State the preparation type.
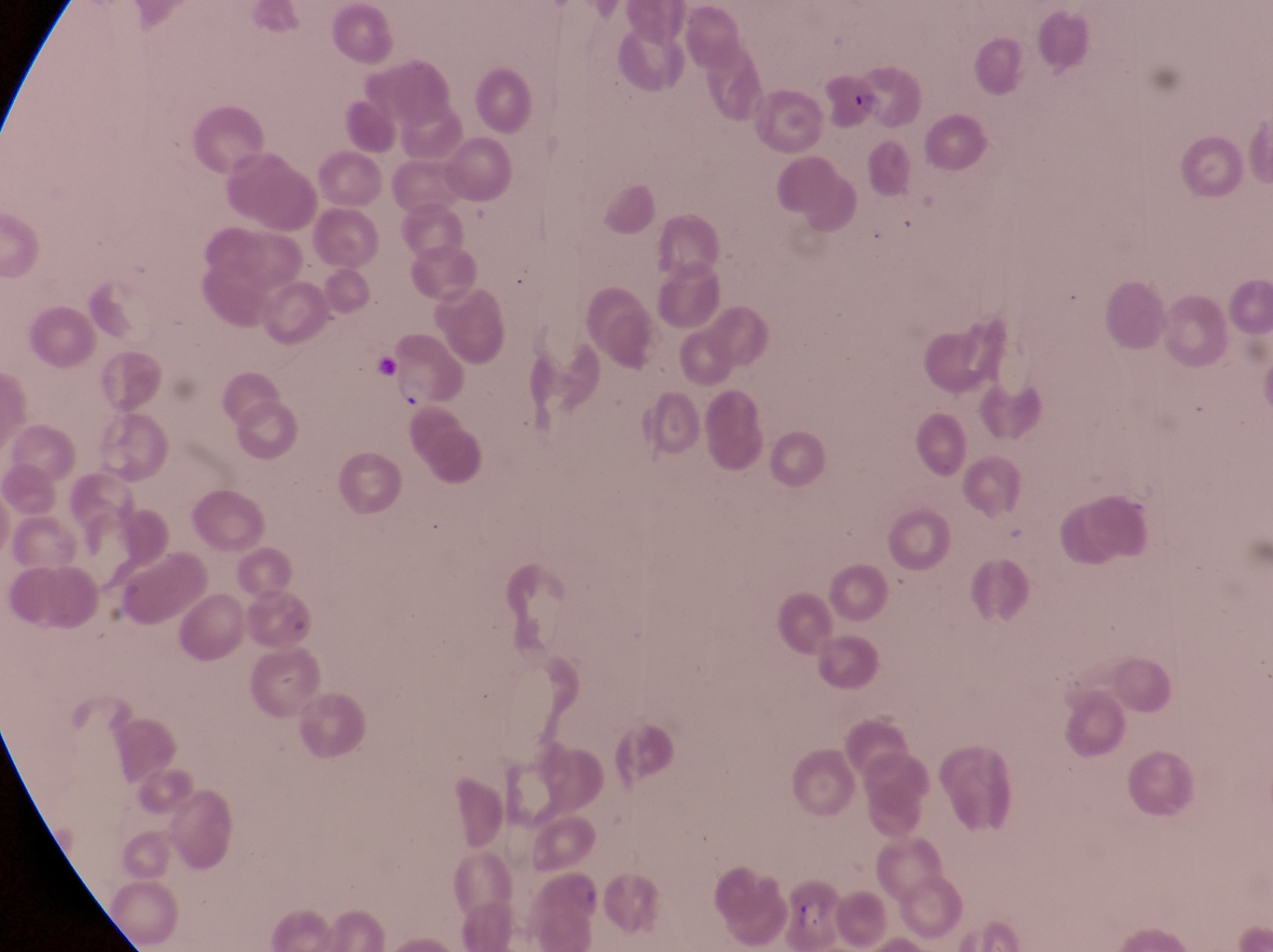

Thin blood film.

Approximate bounding boxes as left top right bottom in pixels. Parasitised red blood cell locations: 847 63 929 131. Trophozoite locations: 391 370 430 412. Image is 1273×952 pixels. Sample from Uganda. One field of view. Photographed through the eyepiece of an Olympus CX-23 microscope with a smartphone camera. At a magnification of 1000x.